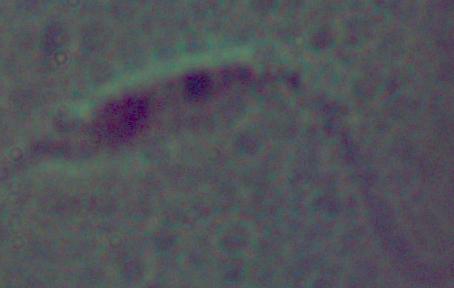

modality: photomicrograph
magnification: 1000x
identification: Leishmania